Assess for Plasmodium parasites.
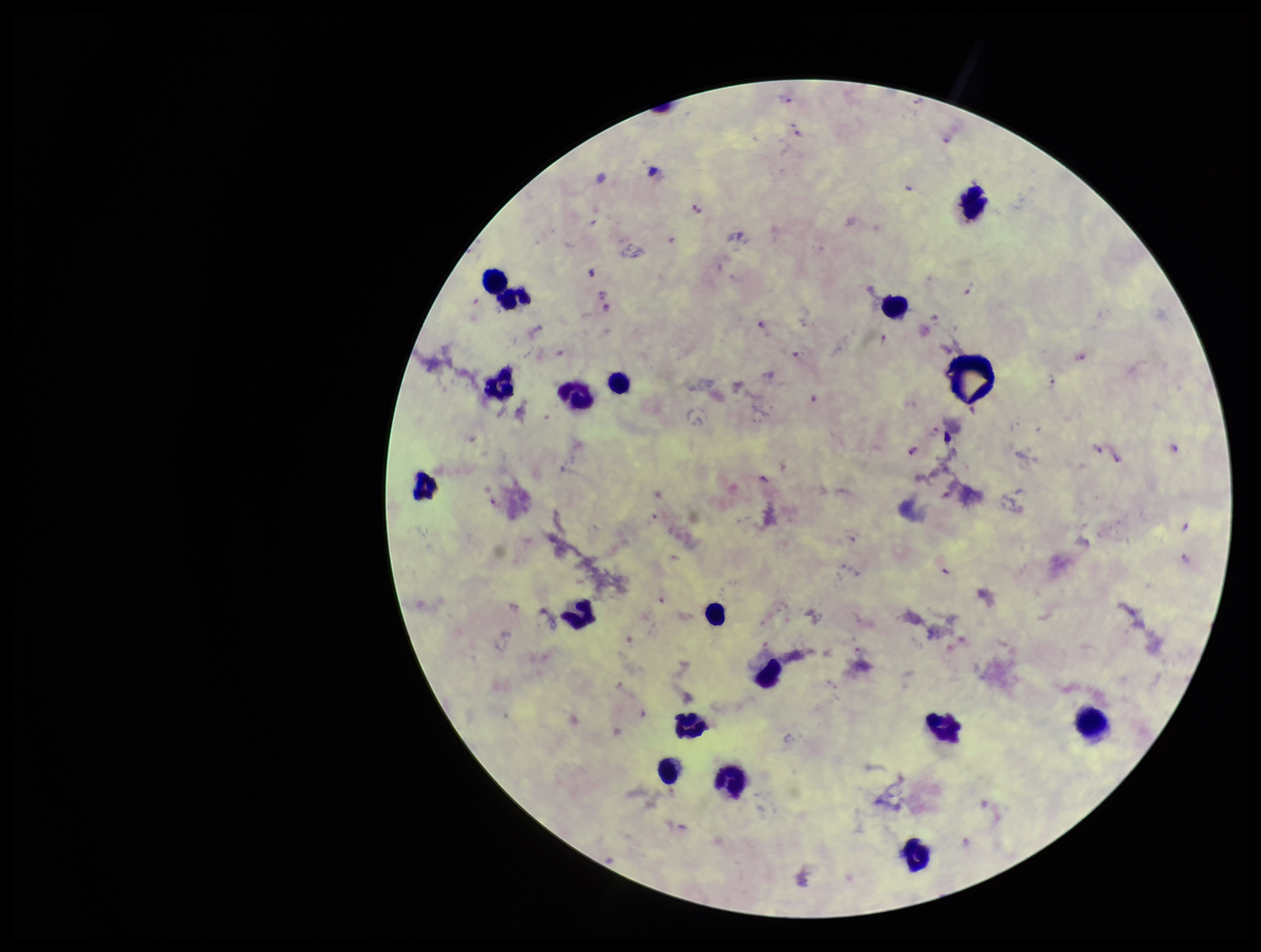

Identified.

Species reported for this patient: Plasmodium falciparum. Patient malaria status: infected. Image is 1261×952 pixels. Single field of view. Parasite count: 19. Giemsa stain. Preparation: thick. Leukocyte count: 18. Smartphone photograph taken through the eyepiece of a microscope.